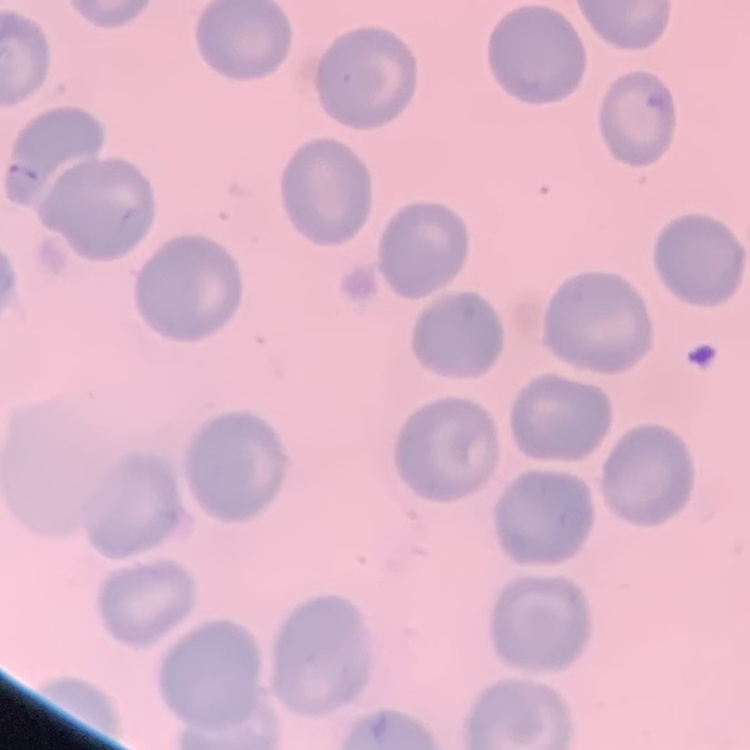
The red blood cells exhibit no rouleaux formation. Thin peripheral smear. Square crop of a larger photomicrograph. Field's or Giemsa stain.